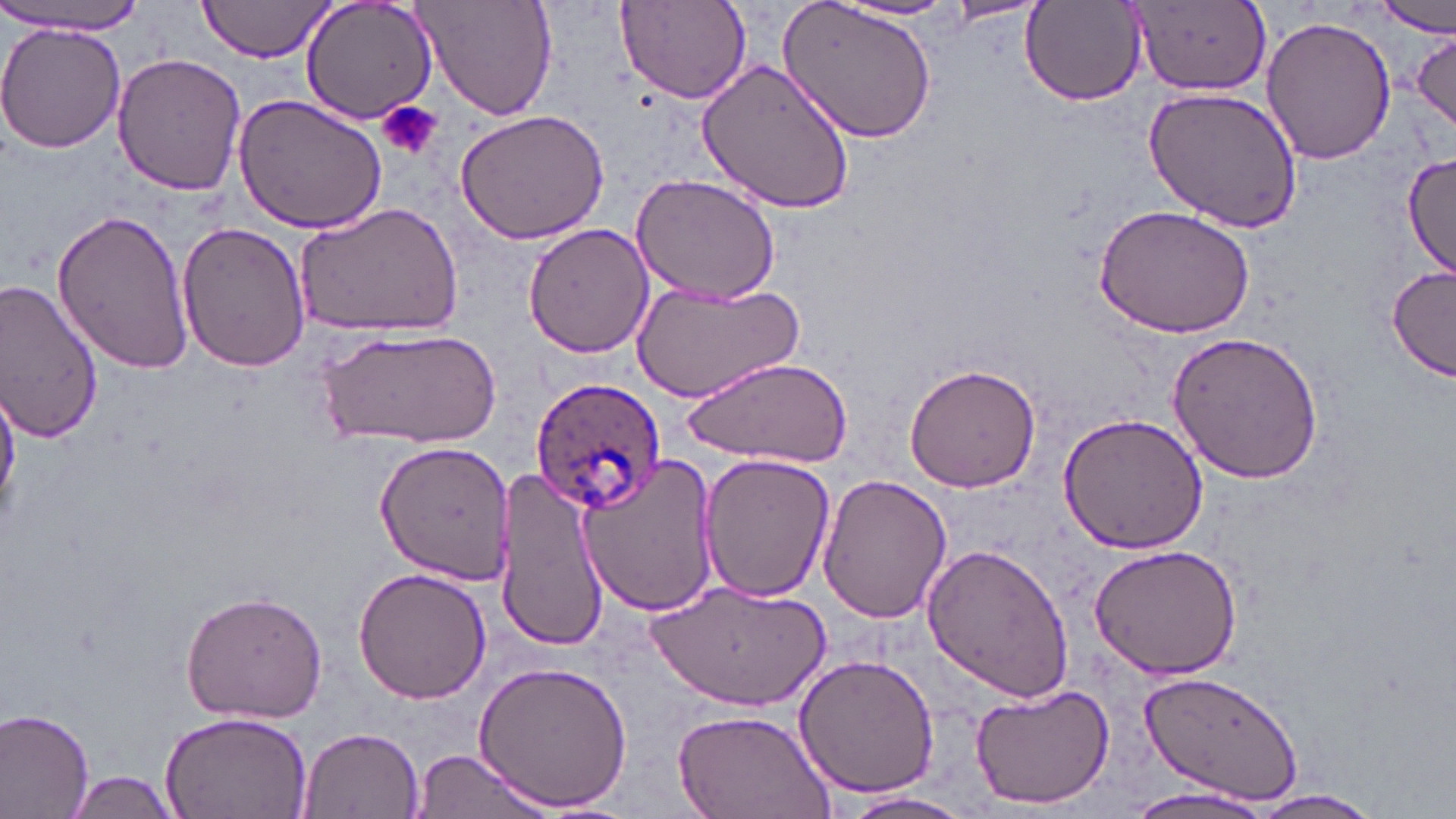 Approximate bounding boxes as (x1,y1)-(x2,y2) corner pairs in pixels. Plasmodium ovale-infected red blood cell locations: (530,377)-(665,514). Uninfected red blood cell locations: (197,0)-(337,62), (299,0)-(441,127), (412,0)-(558,121), (781,0)-(940,142), (615,1)-(752,105), (835,1)-(966,23), (1126,1)-(1272,97), (1373,1)-(1455,38), (1020,3)-(1147,106), (0,6)-(150,35), (1262,14)-(1397,165), (0,23)-(126,155), (1410,30)-(1456,135), (113,53)-(248,195), (697,56)-(858,214), (1143,85)-(1303,233), (232,94)-(388,237), (454,109)-(611,245), (1401,150)-(1456,278), (632,174)-(781,305), (294,201)-(463,340), (1092,204)-(1255,339), (51,208)-(192,375), (176,220)-(311,374), (522,222)-(657,359), (1387,265)-(1454,383), (631,276)-(805,403), (0,281)-(104,442), (321,324)-(501,449), (1165,329)-(1325,484), (689,354)-(854,466), (904,362)-(1041,493), (0,382)-(19,524), (1058,410)-(1210,554), (375,438)-(514,582), (698,454)-(835,601), (576,456)-(720,619), (496,470)-(610,648), (815,472)-(952,625), (922,541)-(1075,704), (1088,543)-(1243,680), (352,568)-(492,704), (646,580)-(831,708), (179,589)-(329,724), (793,654)-(940,799), (473,659)-(633,810), (1137,668)-(1306,806), (968,681)-(1116,810), (0,706)-(95,819), (161,708)-(313,819), (671,710)-(834,819), (297,727)-(425,819), (410,749)-(556,819), (63,770)-(183,818), (1129,785)-(1275,819), (839,790)-(978,818), (1239,790)-(1386,818). Platelet locations: (377,101)-(443,161). Slide-level diagnosis: Plasmodium ovale. May-Grünwald-Giemsa-stained preparation. Single field of view. Captured at 1000x magnification. Thin blood film. Image is 1456×819 pixels. Optical microscopy.